Locate every uninfected red blood cell.
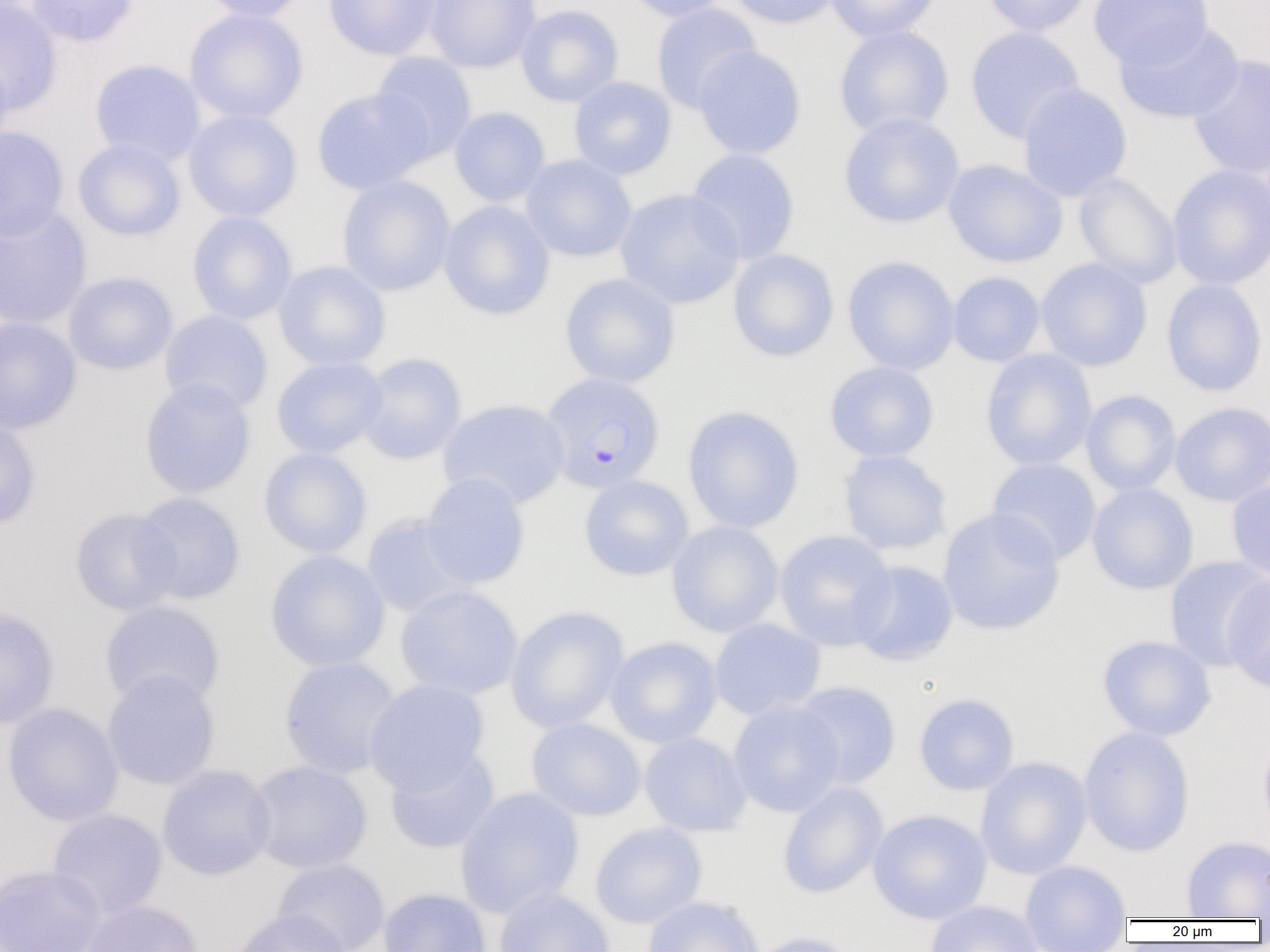

Approximate bounding boxes as [x1, y1, x2, y2] in pixels.
Uninfected red blood cells: [0, 0, 63, 116], [25, 0, 139, 47], [199, 0, 310, 22], [323, 0, 443, 60], [424, 0, 541, 72], [624, 0, 732, 22], [726, 0, 841, 28], [825, 0, 941, 43], [982, 0, 1092, 37], [1088, 0, 1214, 69], [651, 3, 761, 113], [516, 4, 624, 107], [184, 8, 308, 124], [1114, 21, 1245, 124], [833, 26, 954, 138], [965, 26, 1085, 144], [692, 46, 806, 159], [0, 51, 14, 153], [370, 52, 477, 161], [1186, 54, 1270, 179], [89, 59, 206, 165], [569, 76, 677, 179], [1017, 83, 1132, 201], [312, 87, 432, 194], [449, 107, 550, 207], [183, 109, 302, 222], [838, 112, 965, 228], [0, 126, 70, 241], [73, 138, 185, 241], [685, 148, 800, 264], [520, 154, 637, 261], [943, 160, 1068, 268], [1167, 164, 1270, 290], [1074, 173, 1182, 289], [336, 175, 456, 295], [615, 188, 745, 308], [438, 200, 555, 320], [0, 205, 92, 330], [187, 211, 297, 325], [728, 249, 838, 361], [842, 256, 960, 375], [1035, 258, 1152, 371], [274, 261, 391, 371], [63, 271, 178, 375], [947, 272, 1045, 366], [559, 273, 681, 388], [1161, 278, 1268, 397], [159, 310, 273, 414], [0, 316, 82, 434], [980, 349, 1097, 471], [356, 353, 466, 464], [271, 357, 388, 459], [824, 361, 939, 462], [139, 378, 256, 498], [1081, 390, 1181, 496], [438, 399, 570, 509], [1169, 402, 1270, 506], [682, 405, 804, 533], [0, 416, 41, 530], [258, 447, 371, 559], [837, 449, 952, 555], [987, 457, 1101, 565], [420, 472, 530, 589], [579, 475, 694, 580], [1226, 477, 1270, 584], [1087, 483, 1198, 595], [117, 492, 232, 707], [132, 492, 246, 604], [70, 507, 182, 615], [937, 508, 1065, 635], [360, 514, 474, 618], [666, 520, 784, 637], [774, 530, 897, 651], [264, 550, 390, 672], [1165, 555, 1269, 671], [849, 560, 959, 666], [1222, 573, 1270, 694], [395, 584, 523, 700], [100, 600, 225, 710], [504, 606, 629, 733], [0, 608, 59, 730], [708, 618, 825, 719], [1097, 635, 1216, 740], [605, 637, 722, 748], [278, 656, 402, 779], [102, 670, 220, 790], [364, 678, 489, 794], [791, 681, 901, 789], [914, 693, 1019, 795], [727, 698, 845, 817], [1, 702, 123, 827], [526, 718, 646, 821], [1078, 726, 1195, 857], [639, 732, 751, 836], [1257, 732, 1270, 839], [384, 745, 500, 854], [975, 756, 1092, 879], [246, 760, 372, 874], [157, 764, 276, 880], [777, 782, 887, 899], [455, 787, 584, 917], [47, 808, 168, 920], [868, 808, 992, 924], [590, 822, 707, 928], [1181, 835, 1269, 919], [272, 858, 390, 952], [1019, 860, 1130, 951], [0, 864, 106, 952], [494, 887, 615, 952], [378, 888, 491, 952], [642, 896, 762, 952], [80, 899, 203, 951], [925, 900, 1044, 952], [230, 908, 351, 952], [747, 931, 862, 952].

Summary:
  - Plasmodium falciparum-infected red blood cell locations: [539, 375, 663, 497]
  - Slide-level diagnosis: Plasmodium falciparum
  - Magnification: 1000x
  - Field of view: one of a larger specimen
  - Image size: 1270×952 pixels
  - Modality: optical microscopy
  - Preparation: thin blood film